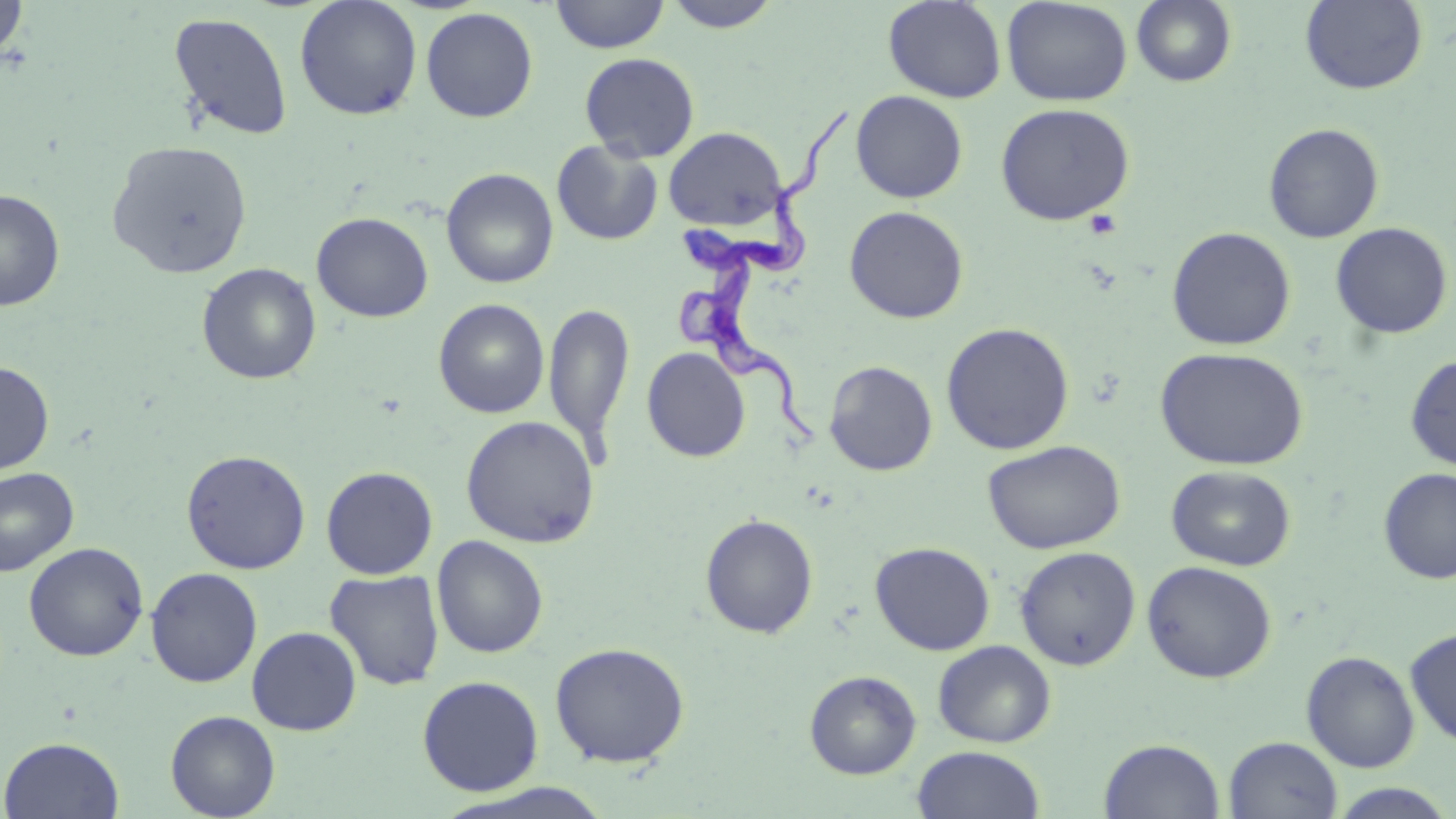 Approximate bounding boxes as (x1, y1, x2, y2) in pixels. Platelet locations: (1084, 209, 1123, 240). Uninfected red blood cell locations: (0, 0, 29, 61), (549, 0, 670, 54), (663, 0, 784, 33), (883, 0, 1006, 103), (1001, 0, 1133, 107), (1131, 0, 1237, 87), (295, 1, 422, 121), (1299, 1, 1428, 95), (420, 7, 538, 122), (168, 11, 293, 142), (579, 52, 700, 163), (850, 90, 968, 203), (995, 103, 1134, 226), (1263, 123, 1384, 243), (662, 126, 788, 231), (106, 140, 253, 279), (551, 140, 664, 246), (441, 168, 559, 288), (0, 190, 65, 311), (844, 205, 969, 324), (311, 212, 433, 322), (1330, 222, 1453, 340), (1167, 226, 1296, 351), (196, 263, 322, 385), (433, 299, 550, 418), (544, 302, 635, 454), (940, 322, 1074, 455), (641, 347, 751, 462), (1155, 347, 1308, 471), (1404, 354, 1456, 471), (0, 360, 54, 475), (824, 360, 938, 476), (460, 415, 600, 548), (983, 440, 1126, 554), (181, 449, 311, 574), (1166, 464, 1297, 571), (321, 466, 438, 579), (0, 467, 79, 577), (1377, 468, 1456, 584), (700, 513, 819, 639), (431, 535, 548, 658), (870, 541, 995, 655), (23, 542, 149, 662), (1015, 546, 1141, 670), (1142, 560, 1277, 683), (146, 567, 263, 687), (325, 569, 445, 690), (247, 626, 362, 735), (1404, 627, 1456, 749), (933, 640, 1057, 748), (549, 641, 690, 768), (1301, 650, 1420, 772), (804, 670, 921, 779), (417, 675, 544, 796), (165, 710, 280, 819), (1223, 736, 1343, 819), (0, 737, 124, 818), (1099, 738, 1225, 819), (912, 745, 1046, 819), (434, 783, 615, 819), (1328, 783, 1455, 818). Trypanosoma brucei locations: (672, 101, 858, 451). Slide-level diagnosis: Trypanosoma brucei. Thin blood smear. Single field of view. 1000x magnification. May-Grünwald-Giemsa stain. Image is 1456×819 pixels. Light microscopy.